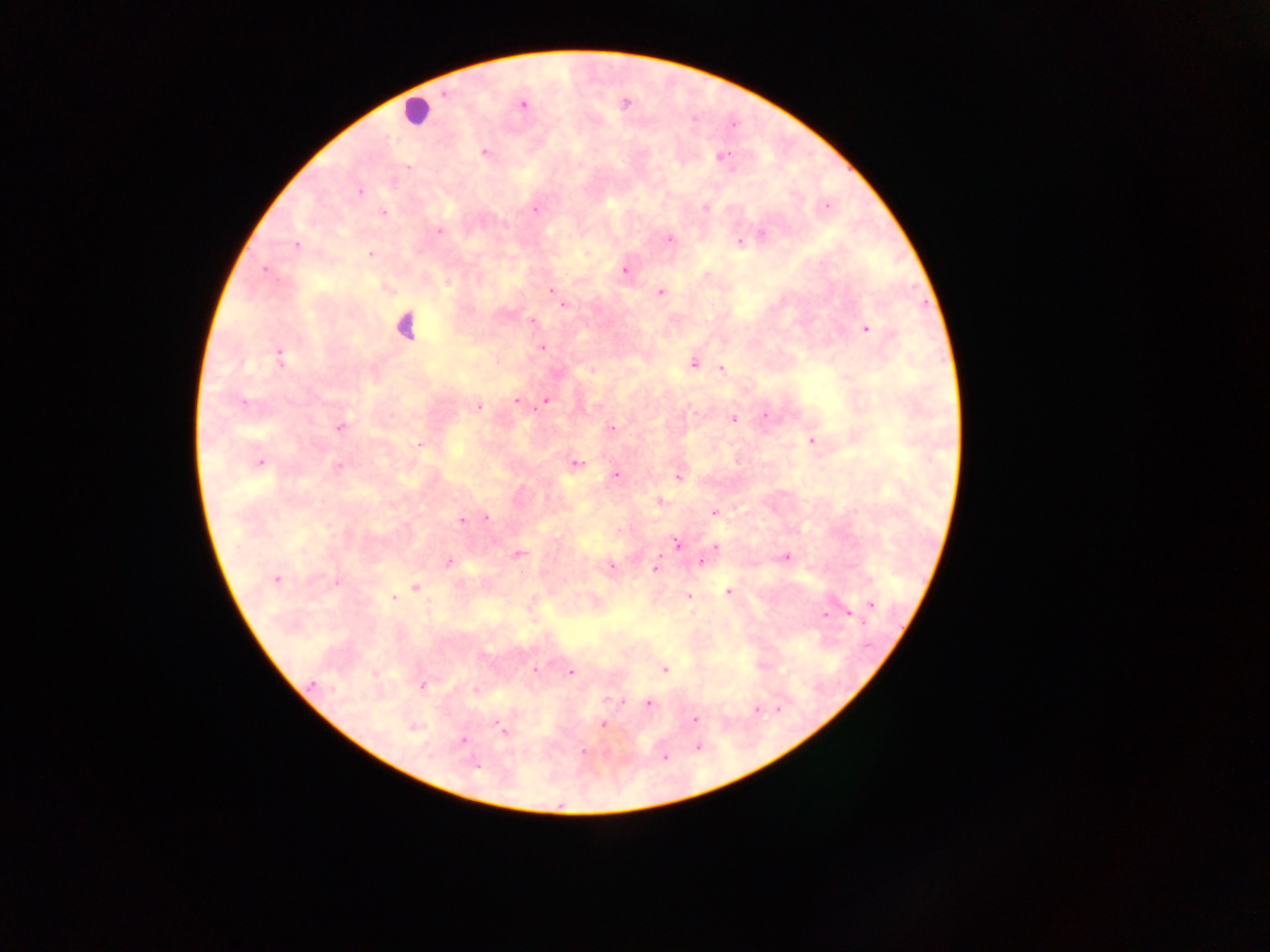
Approximate centers as (x, y) in pixels.
Summary:
  - Plasmodium parasite locations: (443, 94), (625, 104), (523, 105), (694, 119), (485, 152), (723, 156), (408, 167), (359, 191), (826, 205), (706, 208), (536, 210), (383, 213), (439, 231), (761, 234), (669, 239), (739, 242), (297, 245), (370, 254), (265, 269), (625, 270), (553, 290), (660, 292), (557, 296), (563, 304), (532, 321), (865, 328), (542, 348), (279, 356), (694, 364), (721, 369), (545, 400), (517, 401), (244, 403), (478, 406), (765, 416), (733, 419), (340, 428), (611, 428), (812, 442), (420, 445), (260, 462), (576, 463), (338, 467), (616, 475), (679, 477), (659, 502), (714, 513), (487, 516), (462, 521), (677, 544), (715, 546), (518, 554), (786, 557), (449, 561), (701, 562), (611, 565), (656, 567), (276, 579), (336, 583), (415, 588), (728, 591), (393, 597), (689, 597), (871, 605), (825, 614), (850, 615), (664, 669), (534, 670), (571, 672), (313, 684), (423, 686), (476, 690), (648, 704), (756, 709), (694, 719), (603, 724), (503, 730), (462, 741), (698, 748), (583, 752), (665, 757), (475, 767)
  - Leukocyte locations: (417, 111), (405, 326)
  - Image size: 1270×952 pixels
  - Capture: mobile-phone photograph through a microscope
  - Country: Ghana
  - Preparation: thick blood film
  - Field of view: single